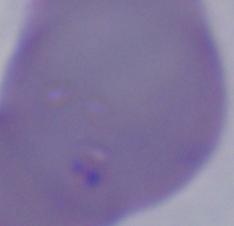

A Babesia parasite is shown. 1000x magnification. Micrograph.